Describe the morphology of the erythrocytes.
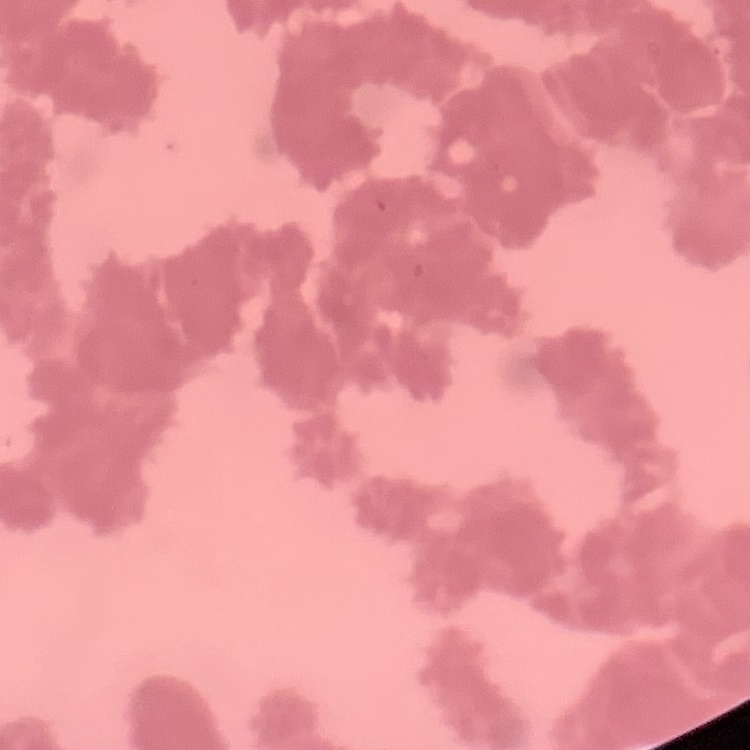
Rouleaux formation.

image type = one tile cut from a larger photomicrograph
preparation = thin blood smear
stain = Field's or Giemsa